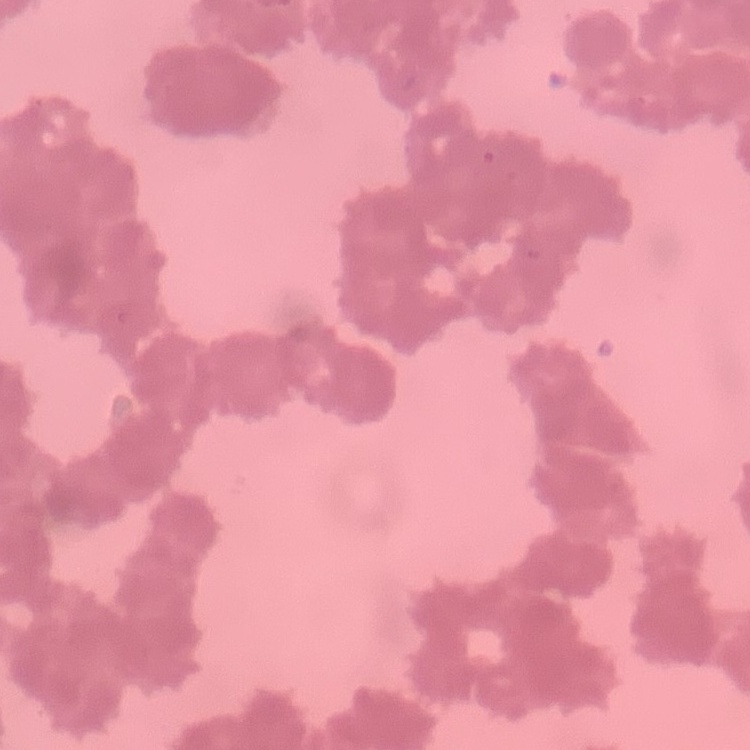

The erythrocytes exhibit rouleaux formation. Stained with either Field's or Giemsa. Thin blood film. Square crop of a larger photomicrograph.